Locate every Plasmodium parasite.
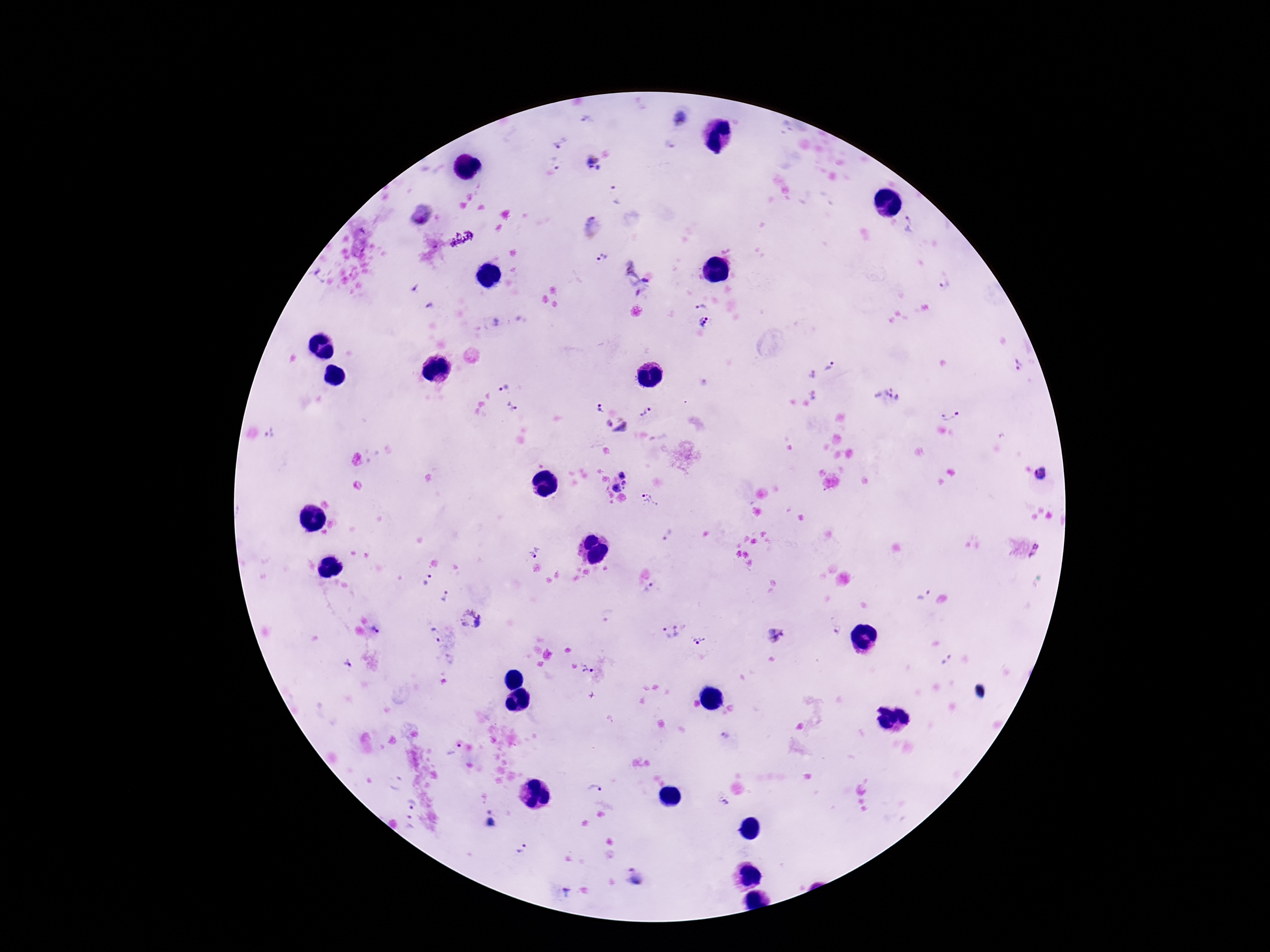

Approximate object centers, in pixels from the top-left corner.
Plasmodium parasites: (x=586, y=119), (x=680, y=119), (x=561, y=142), (x=592, y=159), (x=556, y=163), (x=615, y=196), (x=420, y=215), (x=912, y=218), (x=592, y=228), (x=605, y=258), (x=319, y=275), (x=636, y=279), (x=944, y=282), (x=415, y=289), (x=431, y=306), (x=701, y=308), (x=497, y=321), (x=705, y=323), (x=1019, y=366), (x=832, y=368), (x=811, y=374), (x=502, y=383), (x=812, y=395), (x=887, y=397), (x=512, y=406), (x=599, y=408), (x=644, y=412), (x=950, y=413), (x=607, y=422), (x=623, y=429), (x=272, y=434), (x=1044, y=476), (x=618, y=482), (x=648, y=500), (x=667, y=534), (x=535, y=551), (x=427, y=581), (x=652, y=587), (x=921, y=594), (x=445, y=597), (x=472, y=620), (x=377, y=630), (x=674, y=631), (x=434, y=635), (x=776, y=636), (x=698, y=640), (x=947, y=660), (x=347, y=664), (x=588, y=669), (x=724, y=736), (x=453, y=750), (x=595, y=789), (x=723, y=800), (x=410, y=803), (x=493, y=820), (x=409, y=824), (x=522, y=850), (x=635, y=876).

Summary:
  - Stain: Giemsa
  - Capture: smartphone camera through the microscope eyepiece
  - Preparation: thick blood film
  - Magnification: 100x
  - Patient malaria status: infected
  - Field of view: single
  - Image size: 1270×952 pixels